Classify this cell by malaria status.
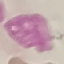
It is uninfected.

Summary:
  - Preparation: thin blood smear
  - Image type: automatically extracted cell patch, resized to 64 × 64 pixels
  - Capture: smartphone through the microscope eyepiece
  - Stain: Giemsa